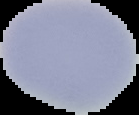
image_type: segmented cell region with the area outside set to black
image_size: 139×115 pixels
result: no Plasmodium parasites seen
preparation: thin blood smear